Report the malaria status of this cell.
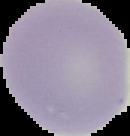
Uninfected.

image size = 130×136 pixels
preparation = thin blood film
image type = segmented cell region with the area outside set to black